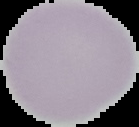

Summary:
  - Image type: segmented cell region on a black background
  - Image size: 139×127 pixels
  - Malaria status: uninfected
  - Preparation: thin blood film